Locate and identify every blood parasite.
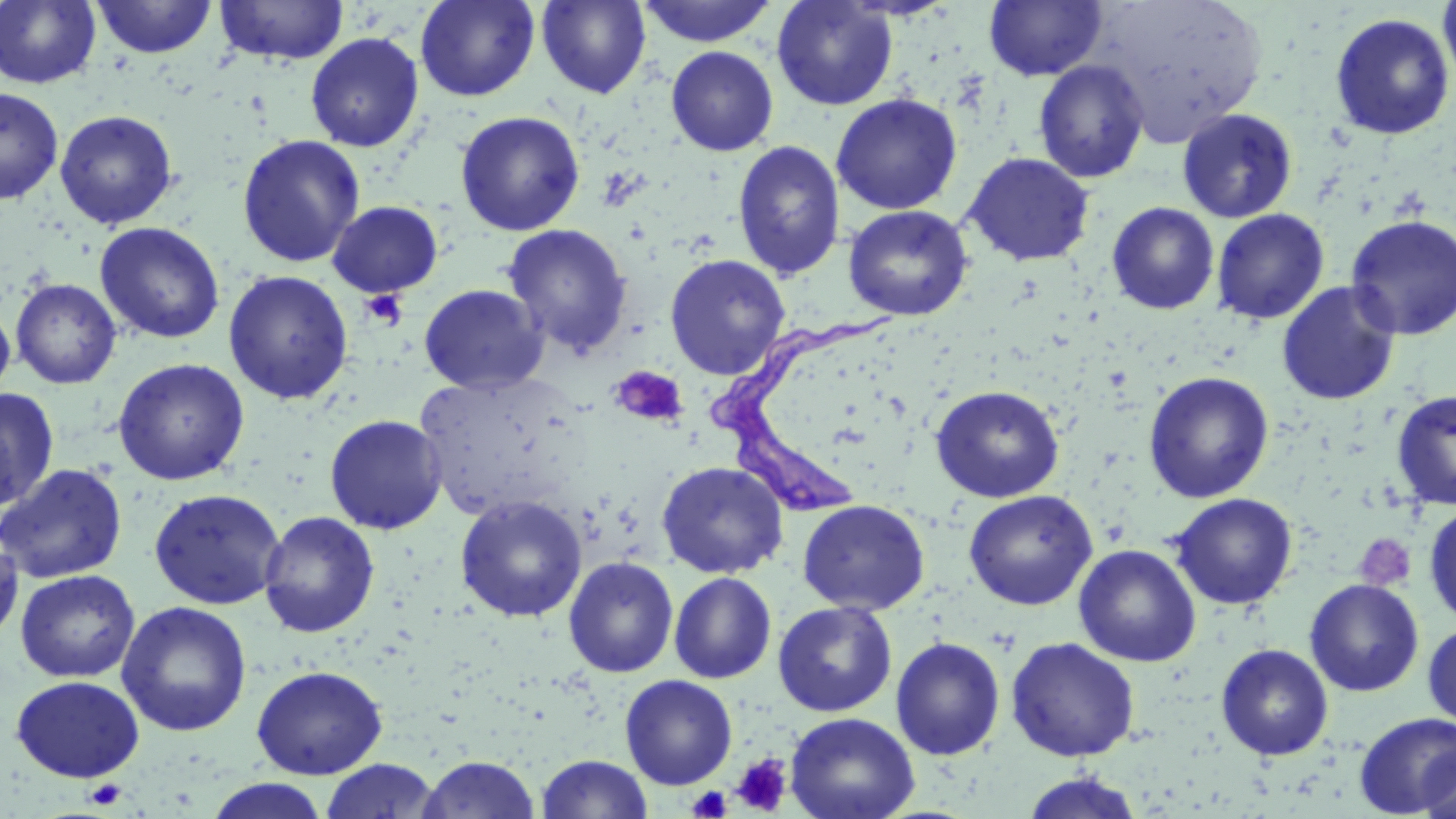
Approximate bounding boxes as named x1/y1/x2/y2 corners in pixels.
Trypanosoma brucei: (x1=709, y1=306, x2=898, y2=513).
No Plasmodium falciparum, Plasmodium ovale, Plasmodium malariae, Plasmodium vivax, or Babesia divergens observed.

Uninfected red blood cell locations: (x1=0, y1=0, x2=100, y2=89), (x1=93, y1=0, x2=216, y2=59), (x1=214, y1=0, x2=349, y2=66), (x1=415, y1=0, x2=540, y2=102), (x1=637, y1=0, x2=777, y2=47), (x1=772, y1=0, x2=897, y2=111), (x1=1092, y1=0, x2=1269, y2=146), (x1=537, y1=1, x2=650, y2=98), (x1=983, y1=1, x2=1107, y2=82), (x1=1438, y1=1, x2=1456, y2=90), (x1=1330, y1=13, x2=1454, y2=140), (x1=305, y1=32, x2=424, y2=152), (x1=666, y1=46, x2=779, y2=157), (x1=1033, y1=59, x2=1150, y2=183), (x1=0, y1=87, x2=63, y2=205), (x1=831, y1=94, x2=962, y2=214), (x1=1176, y1=108, x2=1299, y2=224), (x1=54, y1=110, x2=178, y2=229), (x1=455, y1=111, x2=585, y2=236), (x1=236, y1=134, x2=365, y2=268), (x1=732, y1=140, x2=845, y2=281), (x1=963, y1=152, x2=1094, y2=267), (x1=327, y1=201, x2=443, y2=298), (x1=1107, y1=202, x2=1219, y2=315), (x1=843, y1=205, x2=973, y2=321), (x1=1211, y1=208, x2=1329, y2=325), (x1=1345, y1=215, x2=1456, y2=340), (x1=94, y1=222, x2=225, y2=344), (x1=502, y1=223, x2=632, y2=357), (x1=665, y1=254, x2=791, y2=380), (x1=223, y1=270, x2=353, y2=404), (x1=11, y1=278, x2=122, y2=389), (x1=1277, y1=282, x2=1401, y2=406), (x1=419, y1=284, x2=548, y2=394), (x1=0, y1=300, x2=15, y2=403), (x1=112, y1=358, x2=250, y2=486), (x1=414, y1=370, x2=585, y2=523), (x1=1143, y1=371, x2=1274, y2=503), (x1=930, y1=384, x2=1065, y2=502), (x1=0, y1=388, x2=59, y2=511), (x1=1390, y1=390, x2=1456, y2=510), (x1=324, y1=414, x2=448, y2=534), (x1=656, y1=461, x2=788, y2=578), (x1=0, y1=463, x2=127, y2=584), (x1=148, y1=488, x2=286, y2=610), (x1=964, y1=489, x2=1098, y2=610), (x1=1169, y1=492, x2=1298, y2=610), (x1=455, y1=495, x2=588, y2=622), (x1=797, y1=499, x2=929, y2=614), (x1=1423, y1=502, x2=1456, y2=627), (x1=259, y1=512, x2=379, y2=637), (x1=1, y1=529, x2=23, y2=647), (x1=1074, y1=544, x2=1201, y2=667), (x1=563, y1=557, x2=679, y2=678), (x1=15, y1=570, x2=140, y2=683), (x1=669, y1=572, x2=777, y2=683), (x1=1304, y1=579, x2=1424, y2=697), (x1=116, y1=601, x2=252, y2=737), (x1=773, y1=601, x2=897, y2=717), (x1=1422, y1=621, x2=1456, y2=729), (x1=1006, y1=636, x2=1140, y2=761), (x1=891, y1=637, x2=1006, y2=760), (x1=1216, y1=643, x2=1334, y2=761), (x1=252, y1=665, x2=388, y2=779), (x1=620, y1=674, x2=737, y2=790), (x1=11, y1=675, x2=145, y2=782), (x1=785, y1=712, x2=920, y2=819), (x1=1353, y1=713, x2=1456, y2=816), (x1=1417, y1=743, x2=1455, y2=819), (x1=536, y1=754, x2=652, y2=819), (x1=418, y1=756, x2=538, y2=818), (x1=321, y1=759, x2=440, y2=819), (x1=1019, y1=771, x2=1146, y2=818), (x1=203, y1=778, x2=331, y2=818). Platelet locations: (x1=360, y1=289, x2=407, y2=330), (x1=609, y1=365, x2=689, y2=428), (x1=1354, y1=532, x2=1417, y2=592), (x1=732, y1=753, x2=792, y2=815), (x1=84, y1=779, x2=126, y2=809), (x1=687, y1=786, x2=733, y2=818). Slide-level diagnosis: Trypanosoma brucei. Light microscopy. Single field of view. Image is 1456×819 pixels. Thin blood film. Captured at 1000x magnification. May-Grünwald-Giemsa-stained preparation.